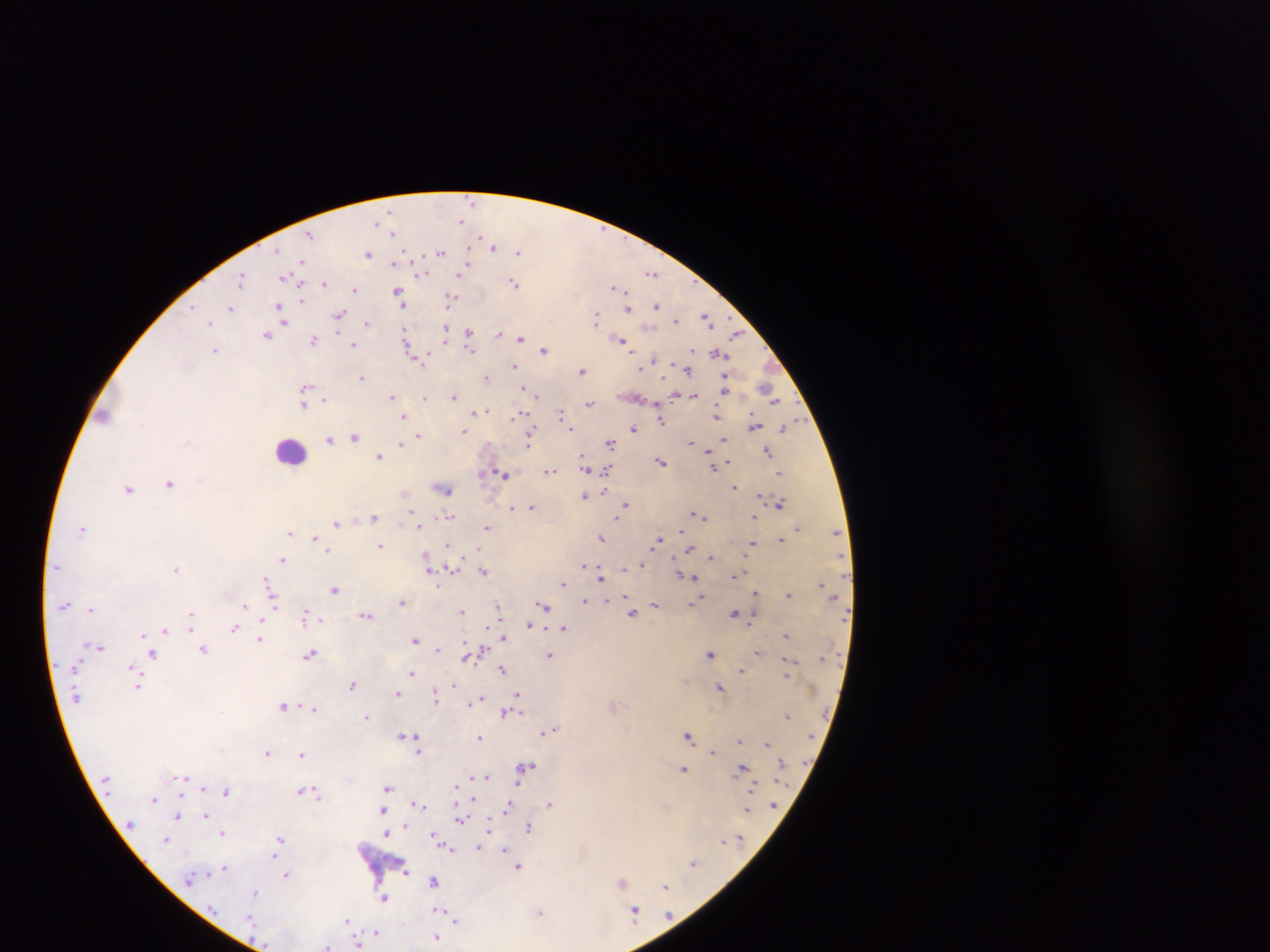

{
  "preparation": "thick blood film",
  "country": "Ghana",
  "field_of_view": "single",
  "leukocyte_locations": "approximate centers as (x, y) in pixels: (291, 450)",
  "image_size": "1270×952 pixels",
  "malaria_parasite_locations": "approximate centers as (x, y) in pixels: (471, 201), (390, 212), (463, 220), (378, 221), (393, 233), (309, 236), (482, 239), (494, 247), (441, 251), (518, 251), (277, 252), (368, 254), (405, 254), (302, 261), (395, 261), (652, 271), (419, 272), (460, 272), (241, 278), (288, 278), (515, 283), (323, 284), (618, 287), (355, 288), (398, 292), (401, 299), (450, 299), (193, 305), (656, 306), (231, 307), (629, 308), (281, 311), (340, 314), (597, 317), (707, 317), (676, 320), (210, 321), (284, 321), (368, 322), (446, 329), (406, 331), (468, 332), (499, 333), (268, 334), (736, 334), (521, 338), (622, 339), (314, 340), (352, 345), (409, 347), (470, 348), (215, 349), (544, 350), (718, 352), (428, 356), (421, 359), (655, 359), (514, 365), (641, 368), (687, 368), (583, 370), (362, 376), (487, 376), (305, 387), (525, 388), (726, 389), (768, 391), (536, 392), (454, 395), (677, 395), (392, 396), (694, 396), (424, 398), (323, 399), (590, 402), (304, 405), (487, 409), (476, 410), (561, 413), (519, 414), (717, 415), (404, 416), (660, 420), (754, 425), (571, 428), (634, 428), (785, 428), (465, 431), (418, 434), (355, 436), (335, 437), (329, 439), (529, 440), (725, 440), (692, 441), (610, 442), (400, 443), (767, 450), (711, 453), (380, 455), (584, 458), (660, 461), (713, 463), (726, 463), (607, 469), (548, 470), (780, 472), (481, 473), (504, 474), (170, 482), (735, 487), (129, 488), (444, 488), (585, 495), (760, 495), (625, 504), (780, 504), (532, 506), (511, 508), (411, 512), (449, 515), (699, 515), (375, 518), (755, 518), (617, 519), (336, 522), (418, 526), (83, 527), (488, 527), (797, 527), (683, 529), (837, 532), (291, 533), (314, 536), (602, 538), (658, 540), (780, 540), (449, 543), (751, 544), (380, 545), (689, 548), (479, 550), (329, 551), (426, 556), (712, 557), (283, 559), (640, 565), (584, 566), (450, 567), (625, 567), (177, 568), (483, 571), (682, 574), (736, 574), (693, 576), (602, 578), (267, 580), (563, 583), (820, 583), (438, 584), (334, 589), (755, 593), (788, 595), (625, 597), (607, 598), (700, 599), (585, 600), (273, 602), (402, 602), (694, 603), (64, 604), (655, 605), (245, 606), (543, 606), (498, 607), (91, 608), (463, 611), (735, 612), (192, 614), (305, 614), (366, 614), (632, 614), (320, 620), (528, 625), (234, 628), (487, 628), (564, 628), (191, 629), (166, 630), (144, 634), (786, 635), (504, 637), (260, 638), (416, 639), (100, 646), (204, 649), (437, 649), (477, 652), (153, 653), (311, 653), (711, 653), (758, 653), (469, 655), (550, 655), (132, 667), (502, 670), (741, 670), (787, 672), (412, 673), (787, 676), (138, 685), (353, 685), (453, 685), (720, 686), (398, 692), (518, 694), (436, 696), (480, 698), (473, 701), (516, 701), (284, 705), (314, 708), (505, 712), (788, 715), (368, 716), (553, 728), (548, 730), (402, 734), (418, 735), (689, 735), (480, 737), (740, 740), (767, 744), (419, 745), (418, 751), (713, 751), (267, 752), (302, 754), (528, 766), (743, 767), (684, 769), (487, 776), (181, 777), (473, 778), (518, 783), (204, 787), (388, 787), (456, 787), (753, 788), (301, 789), (227, 791), (315, 792), (473, 798), (154, 799), (418, 802), (551, 804), (508, 808), (748, 809), (385, 810), (179, 814), (207, 814), (461, 819), (490, 824), (406, 825), (529, 825), (222, 832), (387, 833), (434, 835), (280, 838), (167, 839), (723, 841), (481, 845), (448, 847), (506, 849), (276, 855), (694, 863), (519, 866), (225, 867), (406, 871), (287, 874), (435, 880), (622, 883), (665, 885), (257, 893), (383, 897), (440, 910), (635, 911), (540, 913), (251, 917), (457, 919), (346, 921), (378, 932), (438, 936), (358, 944), (329, 946)",
  "capture": "mobile-phone photograph through a microscope"
}